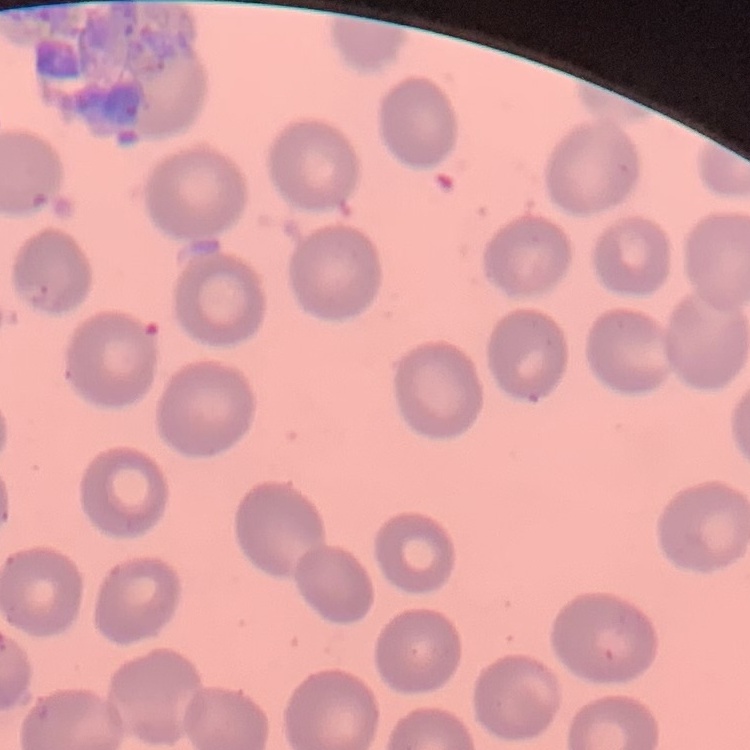 The erythrocytes show no rouleaux formation. One tile cut from a larger photomicrograph. Field's or Giemsa stain. Thin blood film.